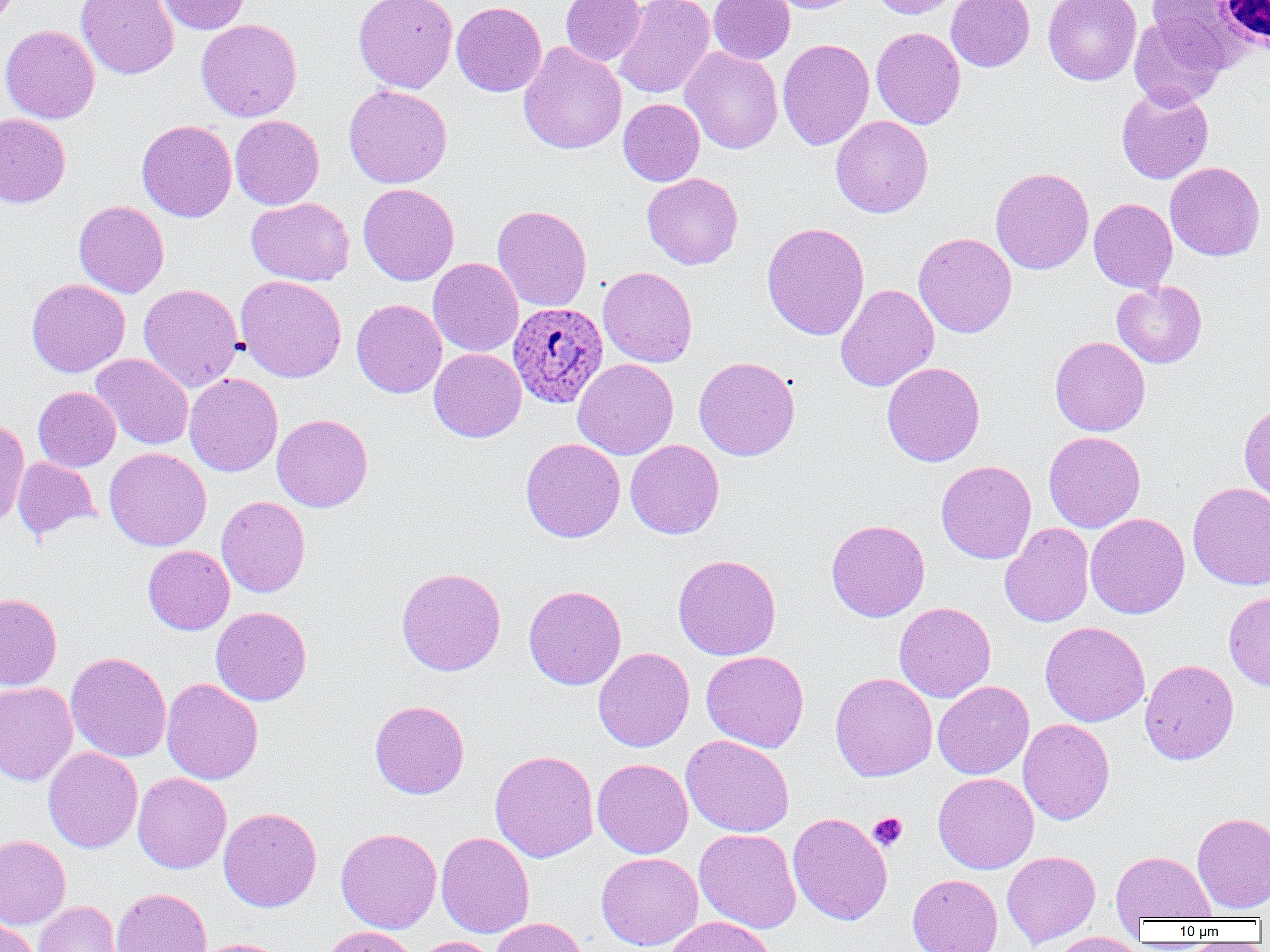
{
  "plasmodium_ovale_infected_red_blood_cell_locations": "approximate bounding boxes as (x1,y1)-(x2,y2) corner pairs in pixels: (507,302)-(608,411)",
  "slide_level_diagnosis": "Plasmodium ovale",
  "image_size": "1270×952 pixels",
  "platelet_locations": "approximate bounding boxes as (x1,y1)-(x2,y2) corner pairs in pixels: (869,812)-(907,851)",
  "magnification": "1000x",
  "modality": "light microscopy",
  "preparation": "thin blood smear",
  "field_of_view": "one of a larger specimen",
  "uninfected_red_blood_cell_locations": "approximate bounding boxes as (x1,y1)-(x2,y2) corner pairs in pixels: (76,0)-(179,80), (157,0)-(250,34), (354,0)-(457,93), (559,0)-(646,66), (613,0)-(715,99), (708,0)-(795,64), (764,0)-(863,13), (870,0)-(960,18), (946,0)-(1035,71), (1145,0)-(1252,64), (451,1)-(547,96), (1043,1)-(1141,85), (1129,14)-(1228,111), (196,19)-(302,122), (0,24)-(100,124), (871,27)-(965,129), (777,39)-(874,150), (518,42)-(627,155), (680,47)-(783,154), (343,84)-(453,189), (1116,89)-(1214,184), (618,98)-(705,186), (0,113)-(71,208), (230,115)-(324,210), (830,115)-(933,218), (137,120)-(237,222), (1165,162)-(1265,261), (990,167)-(1094,275), (642,173)-(743,269), (358,183)-(459,286), (246,197)-(354,286), (1089,198)-(1178,294), (73,200)-(169,298), (492,204)-(592,312), (762,222)-(870,340), (913,232)-(1017,338), (428,257)-(523,357), (598,266)-(697,367), (235,275)-(347,383), (26,278)-(130,377), (1111,280)-(1207,369), (138,283)-(243,392), (836,284)-(939,392), (351,299)-(447,398), (1050,336)-(1150,436), (429,348)-(526,442), (91,353)-(193,450), (693,356)-(800,461), (572,358)-(679,460), (882,362)-(985,467), (184,373)-(283,476), (33,386)-(121,471), (1239,399)-(1270,504), (272,413)-(373,512), (0,419)-(30,530), (1043,431)-(1145,533), (521,438)-(625,543), (625,439)-(724,539), (104,447)-(211,551), (12,457)-(100,541), (936,460)-(1037,564), (1188,482)-(1270,590), (216,496)-(310,598), (1085,513)-(1190,619), (826,519)-(930,622), (1000,523)-(1094,628), (143,545)-(234,635), (673,554)-(781,660), (396,567)-(506,676), (523,585)-(626,690), (1224,592)-(1270,691), (0,593)-(62,691), (894,602)-(996,702), (211,606)-(312,706), (1040,621)-(1150,727), (593,647)-(694,752), (66,651)-(171,762), (701,651)-(809,752), (1139,659)-(1239,765), (830,672)-(938,781), (161,678)-(263,784), (933,680)-(1034,779), (0,681)-(78,786), (369,700)-(470,799), (1018,719)-(1114,824), (681,735)-(794,837), (43,747)-(143,853), (489,750)-(599,862), (592,758)-(693,858), (132,772)-(231,873), (933,773)-(1039,874), (218,807)-(322,912), (788,812)-(892,925), (1192,812)-(1270,913), (336,828)-(441,934), (694,828)-(801,933), (436,832)-(534,938), (0,835)-(71,929), (1002,850)-(1100,948), (1111,851)-(1216,924), (596,852)-(703,950), (908,874)-(1003,952), (110,887)-(212,952), (34,901)-(122,952), (665,916)-(776,952), (490,917)-(589,952), (0,918)-(43,952), (320,925)-(420,952), (1048,932)-(1147,952), (410,936)-(500,952), (192,937)-(289,952)",
  "white_blood_cell_locations": "approximate bounding boxes as (x1,y1)-(x2,y2) corner pairs in pixels: (1215,1)-(1270,52)"
}